Comment on the morphology of the erythrocytes.
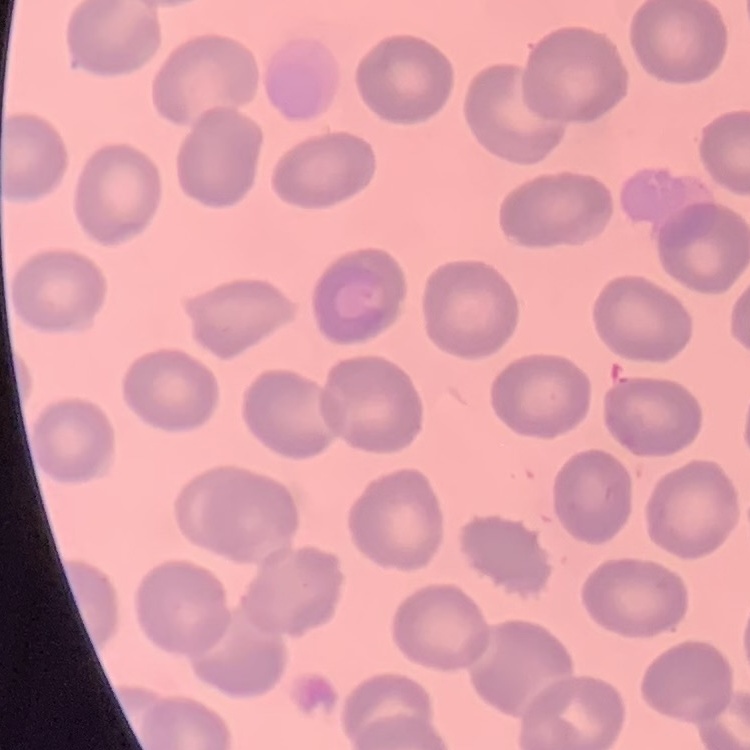

No rouleaux formation.

preparation: thin blood film
stain: Field's or Giemsa
image_type: one tile cut from a larger photomicrograph